Classify this cell by malaria status.
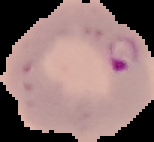

Parasitized.

Summary:
  - Preparation: thin blood smear
  - Image type: segmented cell region with the area outside set to black
  - Image size: 154×142 pixels